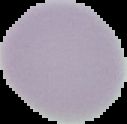

Summary:
  - Image size: 127×124 pixels
  - Image type: segmented cell region with the area outside set to black
  - Preparation: thin blood smear
  - Malaria status: uninfected